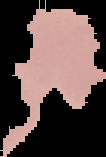
image size = 106×157 pixels
image type = segmented cell region with the area outside set to black
malaria status = uninfected
preparation = thin blood film